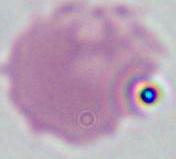

{
  "identification": "red blood cell",
  "magnification": "1000x",
  "modality": "photomicrograph"
}